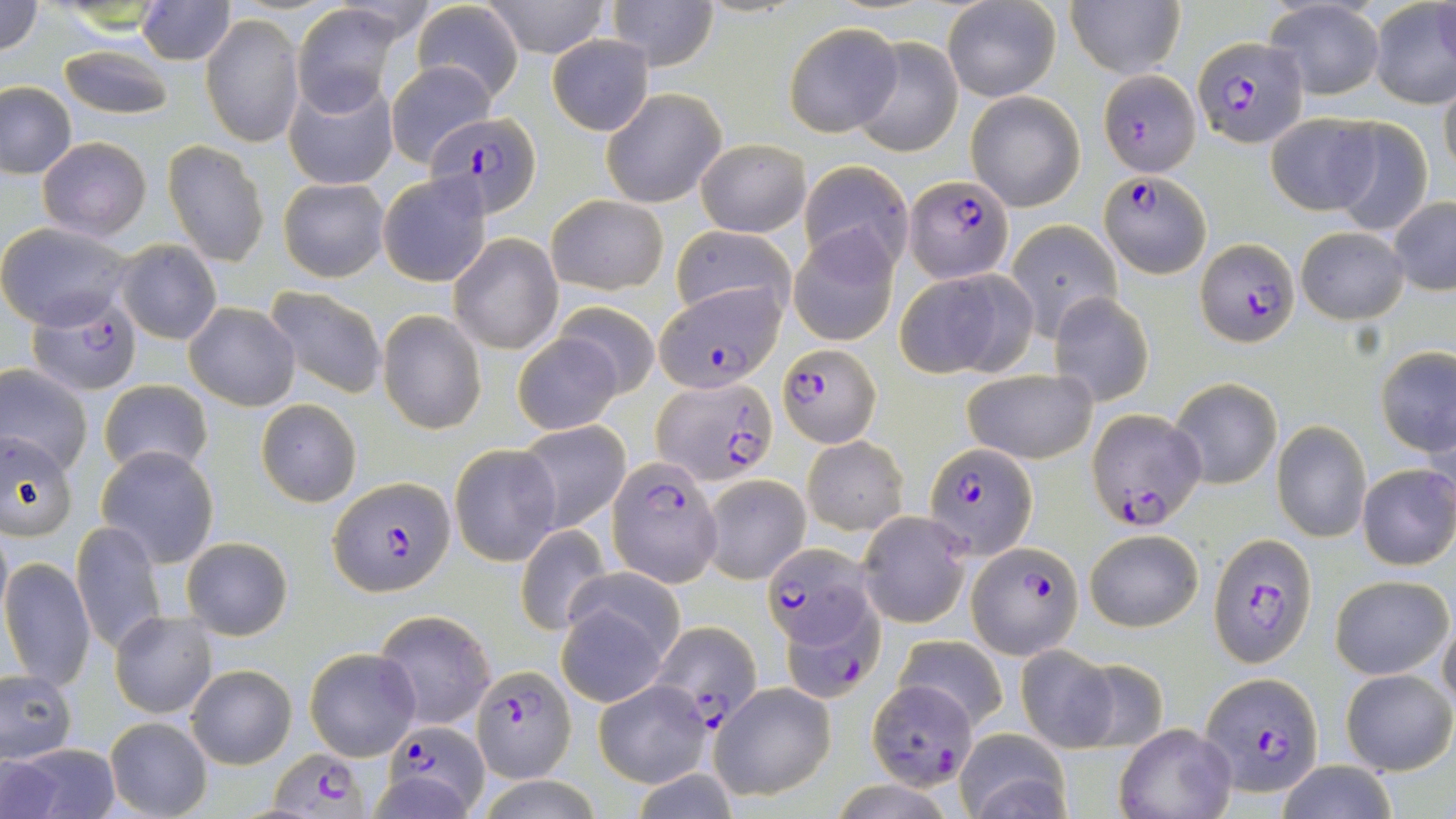
Approximate bounding boxes as [x1, y1, x2, y2] in pixels. Uninfected red blood cell locations: [0, 0, 45, 57], [134, 0, 236, 64], [606, 0, 719, 72], [482, 1, 610, 58], [941, 1, 1062, 103], [1066, 1, 1185, 79], [1264, 1, 1385, 99], [1369, 1, 1456, 107], [411, 3, 524, 100], [293, 5, 401, 117], [202, 14, 304, 147], [783, 21, 902, 137], [547, 36, 653, 134], [849, 36, 962, 156], [57, 43, 176, 120], [386, 61, 495, 164], [285, 78, 398, 190], [1438, 78, 1456, 185], [0, 81, 77, 179], [602, 88, 726, 207], [966, 91, 1085, 211], [1264, 111, 1380, 215], [1329, 117, 1434, 236], [38, 137, 152, 240], [696, 138, 811, 238], [163, 140, 270, 267], [799, 160, 914, 273], [377, 172, 493, 287], [280, 177, 389, 281], [546, 195, 669, 295], [1389, 197, 1456, 296], [1004, 220, 1121, 338], [0, 222, 136, 330], [668, 225, 798, 324], [1295, 225, 1409, 324], [789, 227, 899, 347], [448, 233, 562, 353], [114, 240, 222, 345], [896, 268, 1036, 379], [264, 286, 387, 398], [1048, 291, 1155, 407], [553, 300, 659, 398], [185, 302, 300, 410], [378, 311, 485, 433], [512, 332, 624, 434], [1375, 347, 1456, 458], [0, 363, 94, 475], [960, 367, 1099, 464], [1168, 377, 1284, 489], [98, 379, 212, 476], [256, 398, 362, 507], [512, 420, 632, 536], [1273, 420, 1371, 542], [0, 431, 79, 539], [802, 436, 907, 534], [449, 444, 561, 565], [94, 445, 219, 567], [1357, 464, 1456, 570], [699, 474, 811, 583], [857, 511, 970, 629], [72, 521, 165, 655], [515, 525, 612, 635], [1085, 528, 1203, 632], [182, 537, 293, 640], [0, 556, 95, 692], [1330, 574, 1452, 680], [556, 592, 675, 705], [373, 609, 495, 731], [110, 610, 216, 717], [1438, 614, 1456, 713], [894, 636, 1008, 729], [304, 645, 422, 761], [1015, 646, 1123, 750], [1067, 657, 1170, 752], [186, 664, 295, 768], [1341, 668, 1455, 775], [1, 672, 77, 762], [593, 678, 712, 787], [708, 682, 837, 801], [104, 715, 212, 819], [1114, 723, 1236, 819], [955, 729, 1072, 819], [6, 743, 120, 817], [0, 756, 62, 816], [1275, 759, 1399, 819], [475, 772, 604, 818]. Plasmodium falciparum-infected red blood cell locations: [1191, 35, 1311, 148], [1097, 70, 1202, 175], [432, 113, 539, 216], [1099, 170, 1210, 277], [904, 174, 1013, 283], [1195, 241, 1298, 347], [656, 283, 785, 393], [28, 297, 143, 396], [776, 345, 881, 446], [655, 377, 778, 485], [1088, 407, 1209, 532], [922, 443, 1039, 561], [609, 456, 723, 584], [329, 476, 456, 597], [1208, 534, 1316, 666], [969, 541, 1082, 658], [762, 544, 875, 665], [790, 588, 886, 702], [651, 619, 763, 724], [470, 664, 577, 781], [1201, 672, 1324, 795], [867, 678, 978, 787], [376, 717, 486, 814], [269, 747, 369, 815]. Slide-level diagnosis: Plasmodium falciparum. Image is 1456×819 pixels. Light microscopy. 1000x magnification. Thin blood smear. May-Grünwald-Giemsa stain. Single field of view.